Evaluate for parasitized red blood cells.
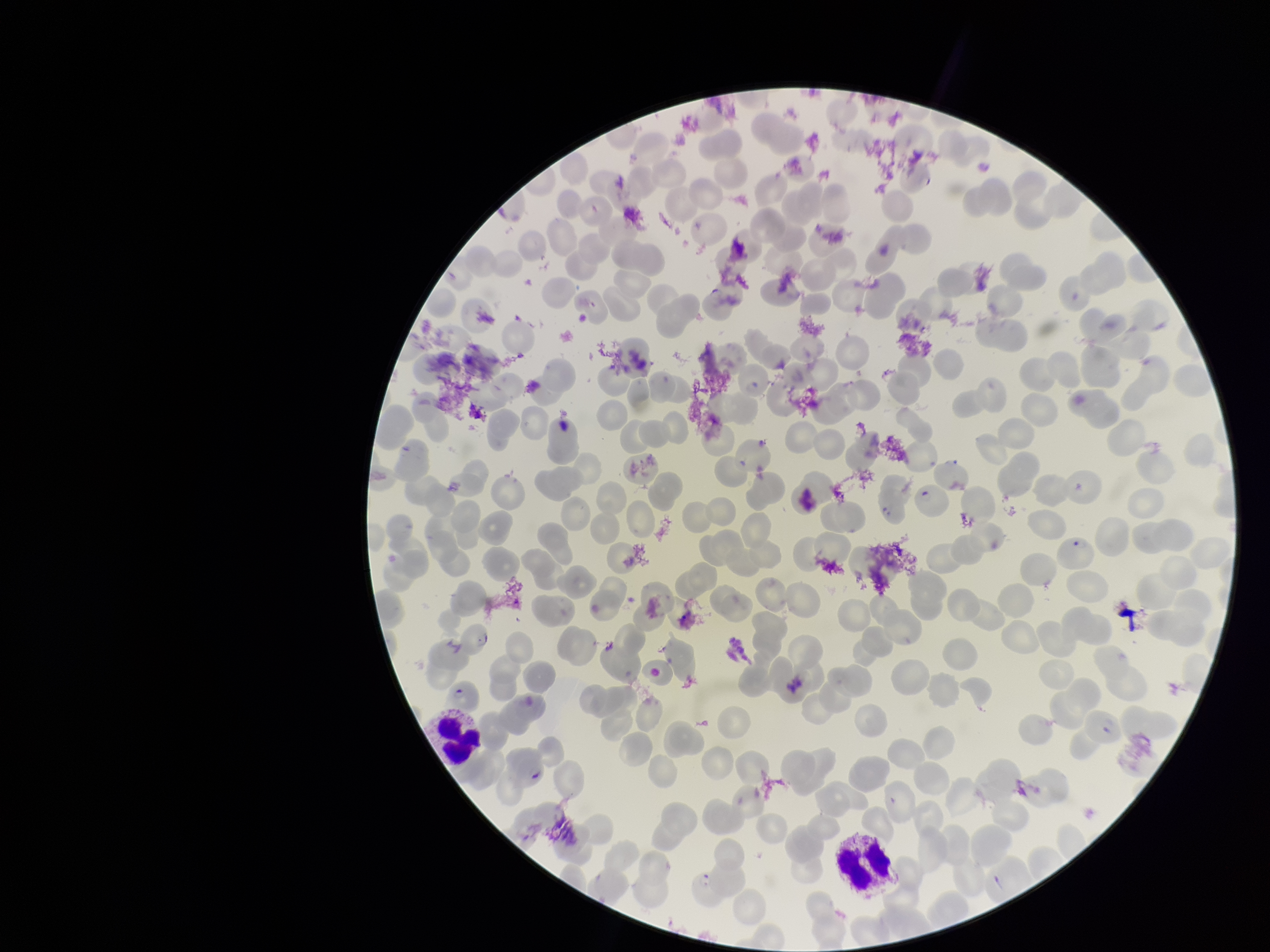
Detected.

Summary:
  - Red blood cell count: 278
  - Field of view: one from this slide
  - Parasitized red blood cell count: 5
  - Stain: Giemsa
  - Patient malaria status: positive
  - Capture: smartphone photograph through the microscope eyepiece
  - Preparation: thin blood smear
  - Image size: 1270×952 pixels
  - Species reported for this patient: Plasmodium falciparum